Classify this cell by malaria status.
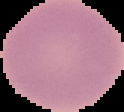

It is uninfected.

Summary:
  - Preparation: thin blood film
  - Image type: cell region segmented out of the field of view; surrounding area masked to black
  - Image size: 124×112 pixels